Report the malaria status of this cell.
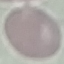

It is uninfected.

Summary:
  - Image type: cell patch, automatically extracted from a larger field of view and resized to 64 × 64 pixels
  - Preparation: thin smear
  - Stain: Giemsa
  - Capture: smartphone camera at the microscope eyepiece